Locate and identify every blood parasite.
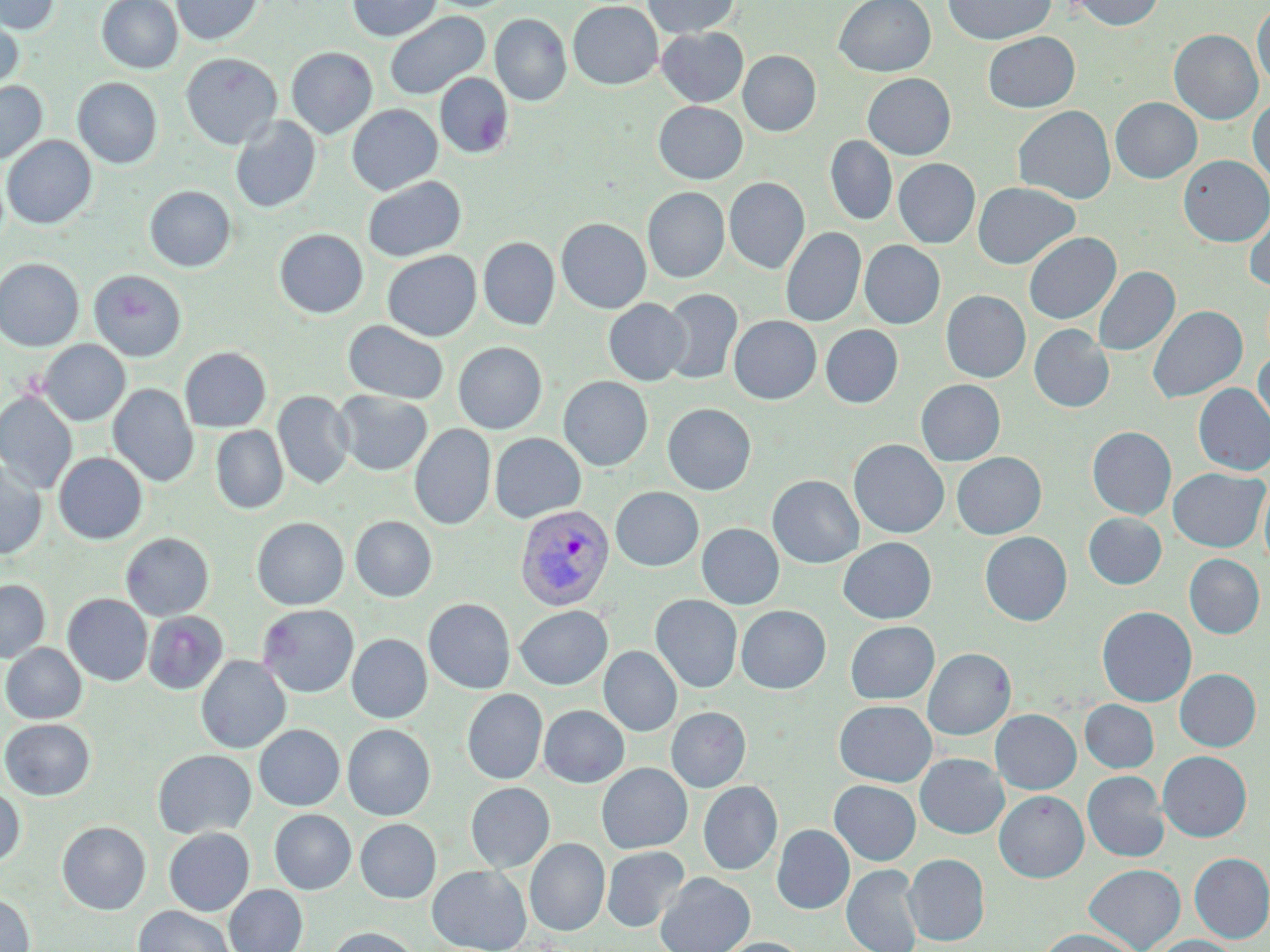
Approximate bounding boxes as (x1, y1, x2, y2) in pixels.
Plasmodium vivax-infected red blood cells: (514, 504, 614, 610).
No Plasmodium falciparum, Plasmodium ovale, Plasmodium malariae, Babesia divergens, or Trypanosoma brucei observed.

Summary:
  - Uninfected red blood cell locations: (0, 0, 60, 35), (96, 0, 182, 73), (172, 0, 263, 45), (346, 0, 442, 42), (643, 0, 740, 38), (834, 0, 936, 77), (944, 0, 1055, 45), (1069, 0, 1166, 30), (568, 1, 663, 90), (1252, 1, 1270, 88), (0, 10, 24, 94), (384, 11, 490, 100), (490, 14, 572, 106), (656, 27, 748, 106), (1169, 29, 1263, 124), (982, 32, 1080, 112), (286, 46, 378, 138), (738, 50, 821, 136), (181, 53, 282, 150), (435, 73, 513, 159), (862, 73, 956, 159), (73, 77, 162, 168), (0, 81, 47, 164), (1110, 97, 1202, 183), (1248, 97, 1270, 185), (653, 101, 748, 184), (346, 104, 442, 195), (1013, 105, 1116, 204), (230, 116, 321, 213), (2, 135, 97, 229), (825, 135, 897, 225), (1179, 155, 1270, 246), (893, 158, 980, 248), (362, 176, 466, 262), (724, 177, 810, 274), (973, 182, 1080, 269), (144, 185, 236, 272), (643, 187, 729, 283), (1244, 204, 1270, 291), (556, 218, 651, 313), (781, 227, 866, 327), (274, 228, 368, 318), (1024, 232, 1120, 324), (478, 237, 559, 330), (860, 240, 945, 329), (382, 250, 481, 341), (0, 257, 84, 351), (1093, 266, 1179, 356), (89, 269, 187, 361), (660, 288, 743, 385), (941, 290, 1030, 382), (604, 299, 690, 386), (1147, 304, 1247, 404), (728, 315, 821, 404), (343, 320, 448, 404), (1029, 324, 1114, 413), (820, 325, 903, 408), (38, 339, 130, 426), (453, 342, 547, 434), (180, 346, 271, 432), (1253, 349, 1270, 440), (558, 376, 653, 471), (916, 379, 1005, 466), (108, 383, 199, 487), (1194, 383, 1270, 475), (0, 390, 77, 494), (335, 390, 432, 475), (273, 391, 354, 490), (663, 403, 756, 495), (410, 424, 495, 530), (211, 426, 288, 513), (1087, 426, 1176, 519), (490, 433, 586, 523), (849, 439, 949, 538), (53, 452, 147, 544), (951, 452, 1046, 539), (0, 461, 47, 559), (1168, 467, 1268, 552), (767, 475, 864, 568), (1259, 478, 1270, 573), (611, 487, 703, 571), (1083, 512, 1167, 589), (350, 516, 437, 602), (251, 517, 349, 610), (697, 523, 784, 609), (980, 531, 1072, 625), (121, 532, 214, 620), (838, 537, 936, 624), (1184, 554, 1264, 638), (0, 579, 50, 662), (63, 594, 152, 685), (650, 594, 742, 694), (424, 599, 515, 694), (257, 604, 359, 697), (515, 605, 612, 689), (736, 605, 830, 693), (1097, 606, 1197, 706), (143, 611, 228, 694), (845, 621, 939, 704), (347, 634, 431, 723), (1, 643, 86, 723), (599, 646, 682, 736), (923, 648, 1016, 740), (196, 656, 291, 753), (1174, 669, 1260, 751), (462, 689, 547, 784), (1080, 699, 1159, 773), (834, 700, 937, 787), (539, 705, 629, 787), (666, 707, 751, 792), (991, 709, 1081, 794), (0, 718, 95, 800), (254, 724, 344, 810), (343, 724, 435, 820), (153, 749, 256, 838), (1157, 751, 1252, 842), (915, 753, 1009, 839), (597, 763, 693, 853), (1082, 771, 1169, 862), (829, 780, 921, 865), (698, 781, 783, 875), (465, 782, 555, 872), (0, 785, 25, 868), (995, 790, 1088, 882), (270, 809, 356, 894), (355, 818, 440, 903), (57, 821, 151, 914), (772, 824, 854, 914), (164, 827, 254, 916), (525, 838, 610, 936), (601, 846, 689, 932), (904, 853, 989, 945), (1189, 853, 1270, 942), (842, 864, 923, 952), (1085, 864, 1185, 952), (427, 865, 532, 952), (656, 872, 755, 952), (224, 885, 307, 952), (0, 893, 35, 952), (133, 906, 235, 952), (325, 927, 423, 952), (1036, 928, 1143, 952), (1145, 935, 1240, 952), (713, 937, 811, 952)
  - Slide-level diagnosis: Plasmodium vivax
  - Preparation: thin blood film
  - Modality: light microscopy
  - Stain: May-Grünwald-Giemsa
  - Magnification: 1000x
  - Field of view: single
  - Image size: 1270×952 pixels